Give the position of every Plasmodium parasite visible.
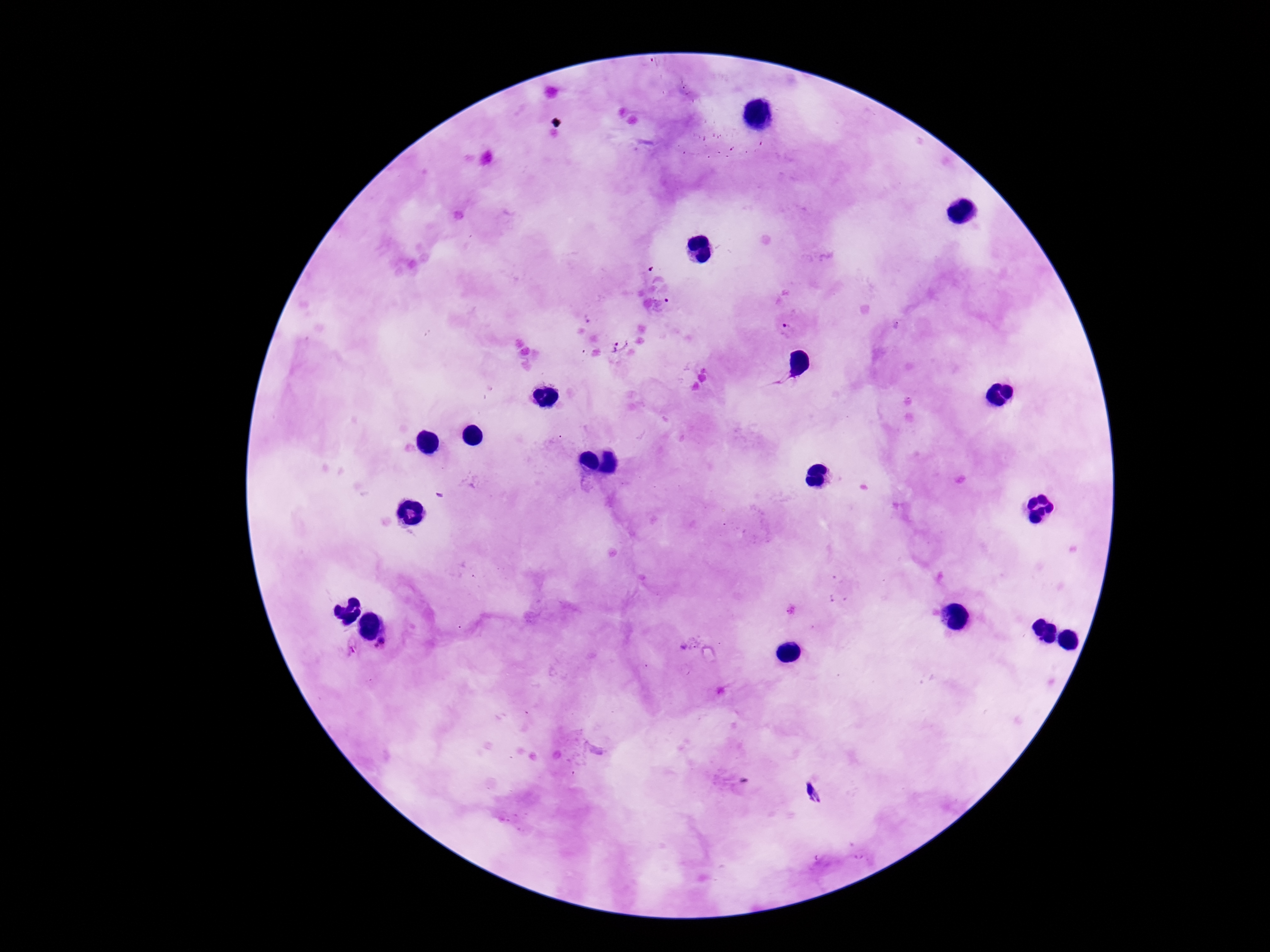

Approximate centers as {x, y} in pixels.
Plasmodium parasites: {787, 327}, {621, 344}, {382, 645}, {349, 646}.

Summary:
  - Image size: 1270×952 pixels
  - Field of view: single
  - Preparation: thick blood smear
  - Patient malaria status: infected
  - Magnification: 100x
  - Capture: smartphone camera through the microscope eyepiece
  - Stain: Giemsa